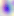
modality = photomicrograph
identification = Toxoplasma gondii
magnification = 400x